Give the preparation type.
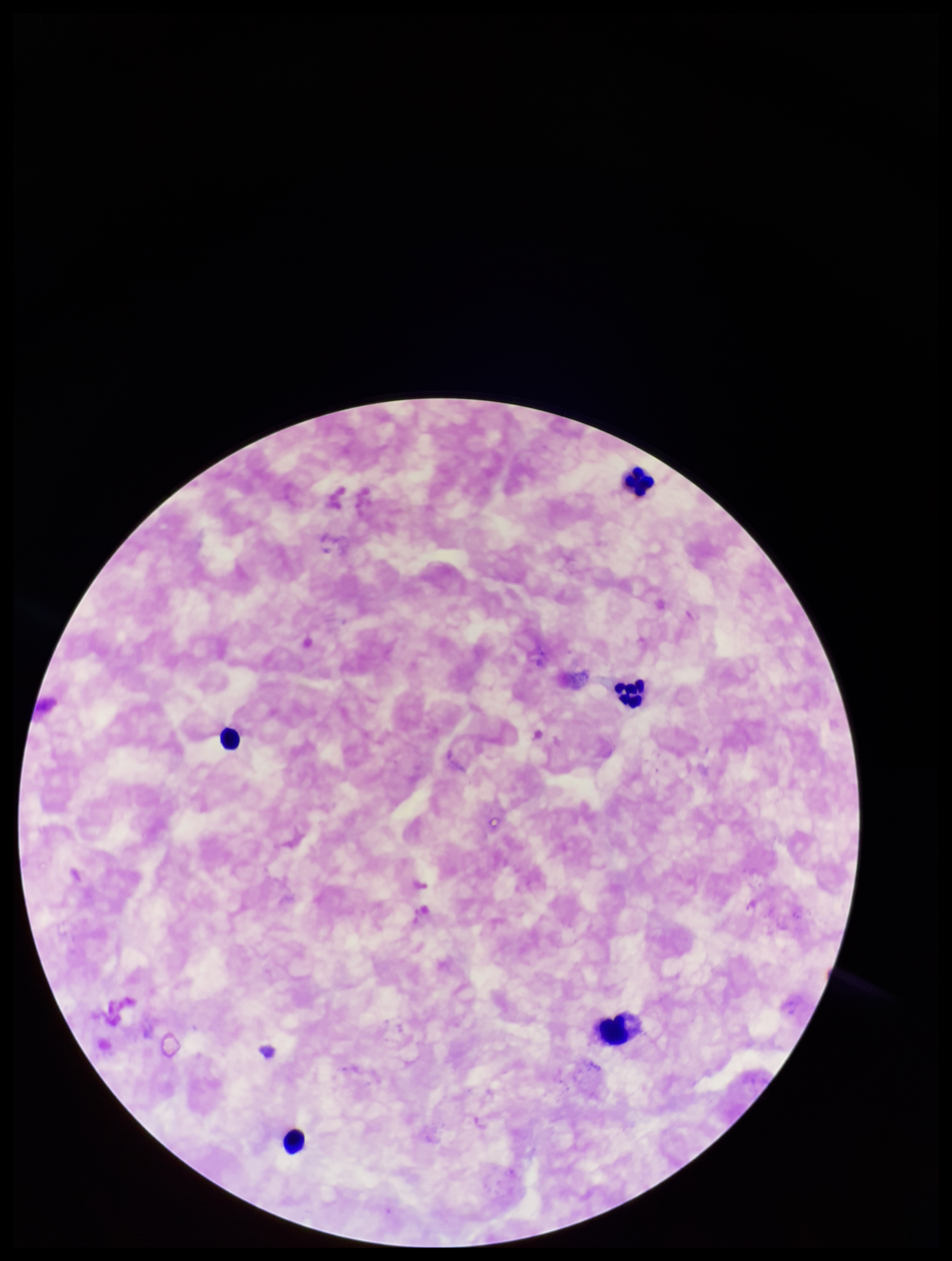

It is a thick blood smear.

{
  "plasmodium_parasites": "none identified",
  "parasite_count": 0,
  "capture": "smartphone photograph through the microscope eyepiece",
  "image_size": "952×1261 pixels",
  "field_of_view": "one from this slide",
  "leukocyte_count": 5,
  "stain": "Giemsa",
  "patient_malaria_status": "negative"
}